Classify this cell by malaria status.
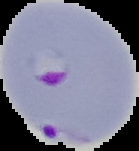
It is parasitized.

Image is 139×151 pixels. The area outside the segmented cell region is set to black. From a thin blood film.